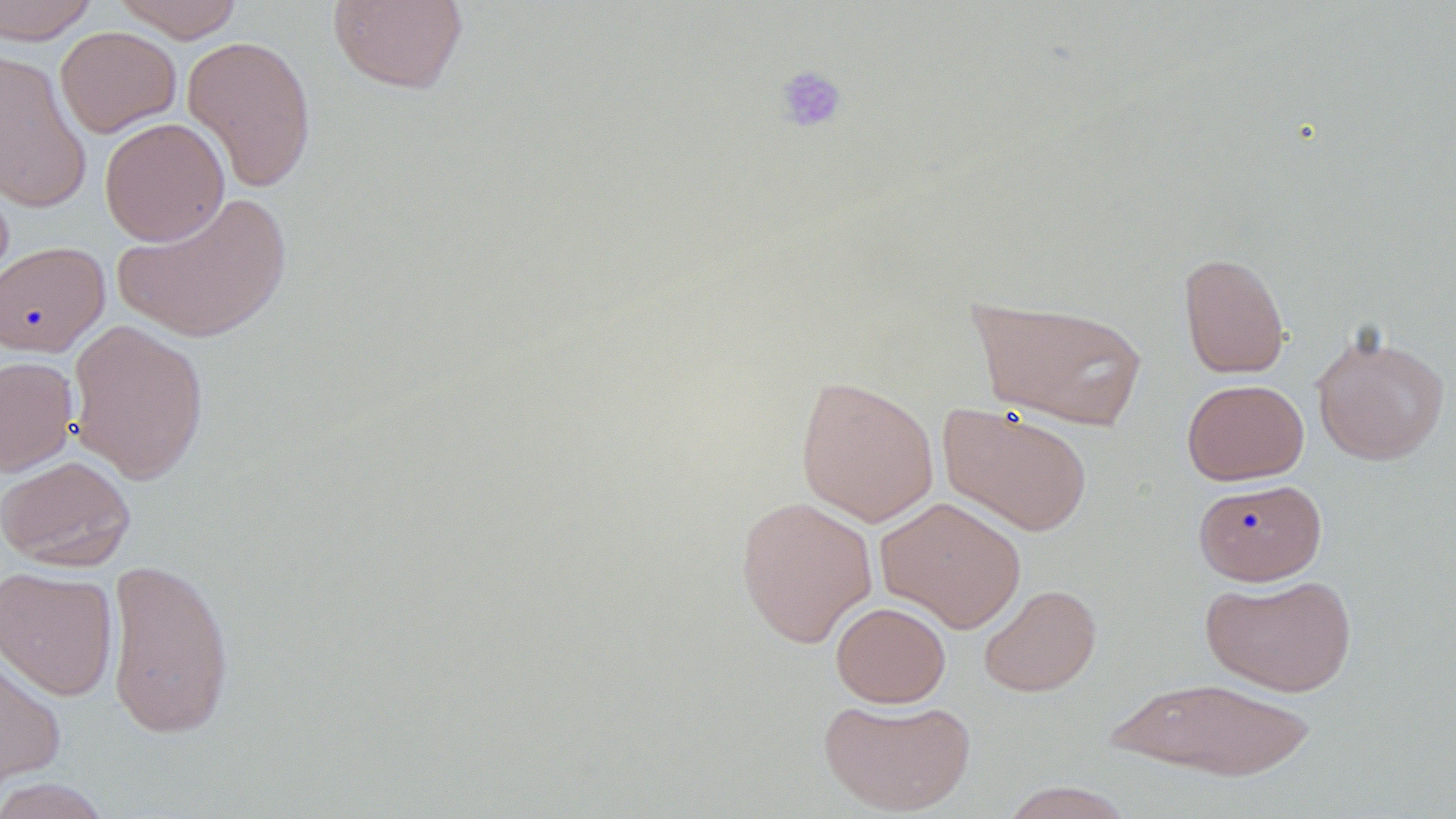

slide-level diagnosis = negative for blood parasites
uninfected red blood cell locations = approximate bounding boxes as named x1/y1/x2/y2 corners in pixels: (x1=0, y1=0, x2=100, y2=44), (x1=112, y1=0, x2=246, y2=42), (x1=327, y1=0, x2=469, y2=95), (x1=55, y1=26, x2=181, y2=137), (x1=182, y1=34, x2=317, y2=194), (x1=0, y1=51, x2=92, y2=212), (x1=99, y1=117, x2=230, y2=246), (x1=113, y1=191, x2=293, y2=344), (x1=0, y1=240, x2=111, y2=357), (x1=1178, y1=252, x2=1291, y2=379), (x1=969, y1=296, x2=1149, y2=430), (x1=67, y1=319, x2=210, y2=485), (x1=1311, y1=328, x2=1451, y2=466), (x1=0, y1=356, x2=78, y2=476), (x1=795, y1=375, x2=939, y2=526), (x1=1181, y1=378, x2=1309, y2=485), (x1=937, y1=403, x2=1092, y2=537), (x1=0, y1=455, x2=136, y2=571), (x1=1193, y1=478, x2=1327, y2=585), (x1=735, y1=495, x2=879, y2=648), (x1=875, y1=496, x2=1027, y2=633), (x1=105, y1=557, x2=236, y2=740), (x1=0, y1=565, x2=119, y2=701), (x1=1200, y1=573, x2=1358, y2=696), (x1=979, y1=583, x2=1102, y2=697), (x1=830, y1=601, x2=951, y2=708), (x1=0, y1=646, x2=66, y2=795), (x1=1102, y1=675, x2=1318, y2=781), (x1=818, y1=695, x2=976, y2=816), (x1=1, y1=776, x2=120, y2=818), (x1=999, y1=781, x2=1135, y2=819)
image size = 1456×819 pixels
preparation = thin blood film
platelet locations = approximate bounding boxes as named x1/y1/x2/y2 corners in pixels: (x1=774, y1=64, x2=848, y2=134)
modality = optical microscopy
magnification = 1000x
stain = May-Grünwald-Giemsa
field of view = one of a larger specimen